Locate and identify every blood parasite.
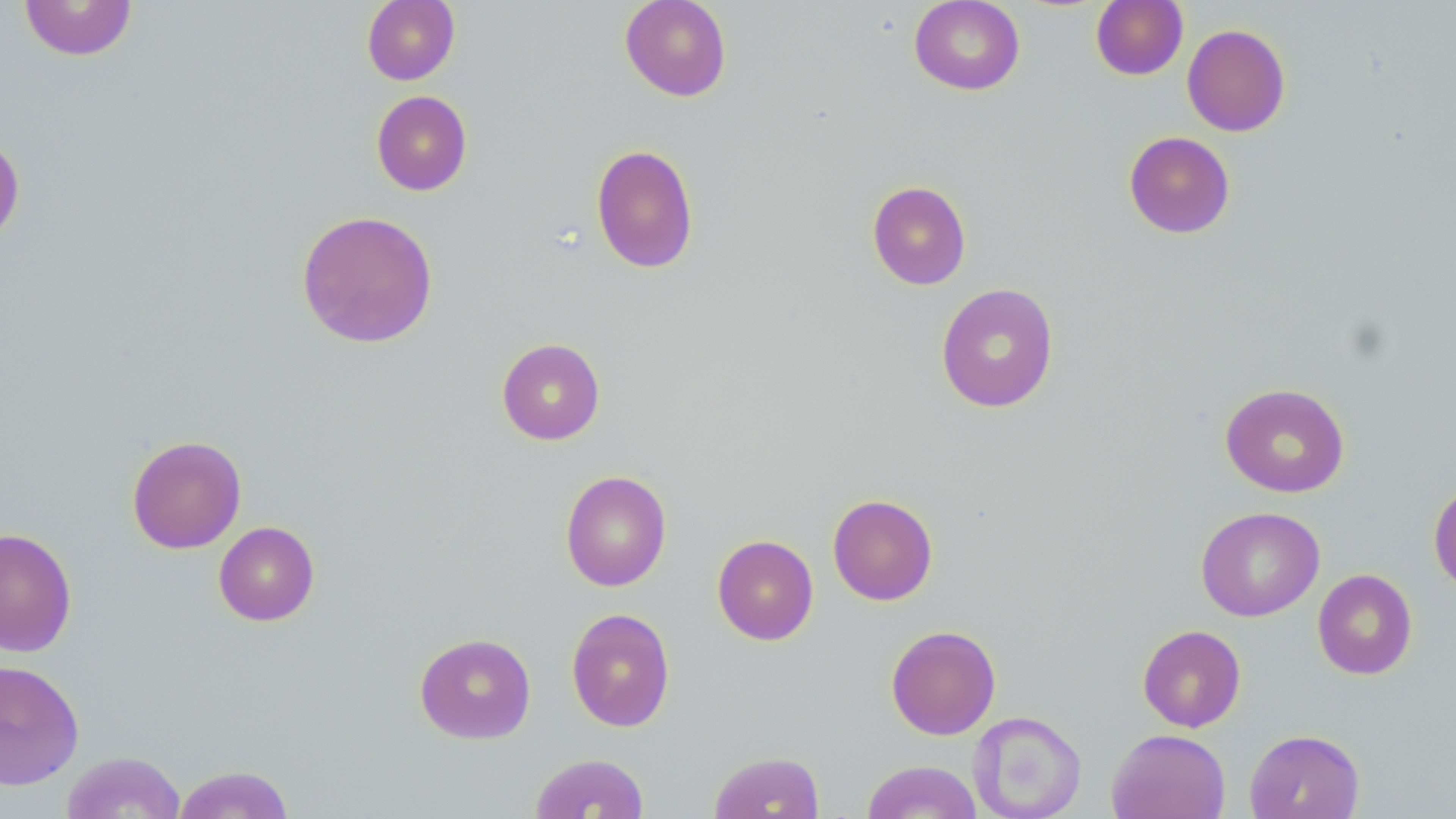
No blood parasites observed.

Summary:
  - Coordinate format: approximate bounding boxes as named x1/y1/x2/y2 corners in pixels
  - Uninfected red blood cell locations: (x1=19, y1=0, x2=137, y2=61), (x1=361, y1=0, x2=460, y2=85), (x1=620, y1=0, x2=732, y2=101), (x1=909, y1=0, x2=1026, y2=95), (x1=1090, y1=1, x2=1188, y2=80), (x1=1182, y1=23, x2=1291, y2=137), (x1=371, y1=90, x2=473, y2=196), (x1=0, y1=131, x2=25, y2=247), (x1=1123, y1=131, x2=1236, y2=238), (x1=590, y1=144, x2=699, y2=274), (x1=867, y1=181, x2=971, y2=290), (x1=296, y1=209, x2=438, y2=349), (x1=935, y1=283, x2=1059, y2=413), (x1=496, y1=338, x2=605, y2=445), (x1=1219, y1=383, x2=1350, y2=497), (x1=127, y1=435, x2=247, y2=553), (x1=560, y1=470, x2=672, y2=591), (x1=1428, y1=480, x2=1456, y2=595), (x1=827, y1=494, x2=938, y2=606), (x1=1196, y1=506, x2=1324, y2=622), (x1=213, y1=521, x2=320, y2=626), (x1=0, y1=527, x2=77, y2=658), (x1=712, y1=534, x2=819, y2=645), (x1=1313, y1=569, x2=1417, y2=680), (x1=566, y1=607, x2=676, y2=732), (x1=886, y1=624, x2=1001, y2=740), (x1=1137, y1=624, x2=1246, y2=732), (x1=414, y1=632, x2=537, y2=744), (x1=0, y1=658, x2=85, y2=791), (x1=968, y1=710, x2=1087, y2=818), (x1=1107, y1=728, x2=1231, y2=819), (x1=1244, y1=729, x2=1365, y2=819), (x1=62, y1=750, x2=186, y2=819), (x1=708, y1=751, x2=825, y2=818), (x1=529, y1=752, x2=650, y2=818), (x1=860, y1=760, x2=983, y2=819), (x1=173, y1=764, x2=296, y2=818)
  - Slide-level diagnosis: no evidence of blood parasites
  - Preparation: thin blood smear
  - Magnification: 1000x
  - Field of view: one of a larger specimen
  - Image size: 1456×819 pixels
  - Modality: optical microscopy
  - Stain: May-Grünwald-Giemsa